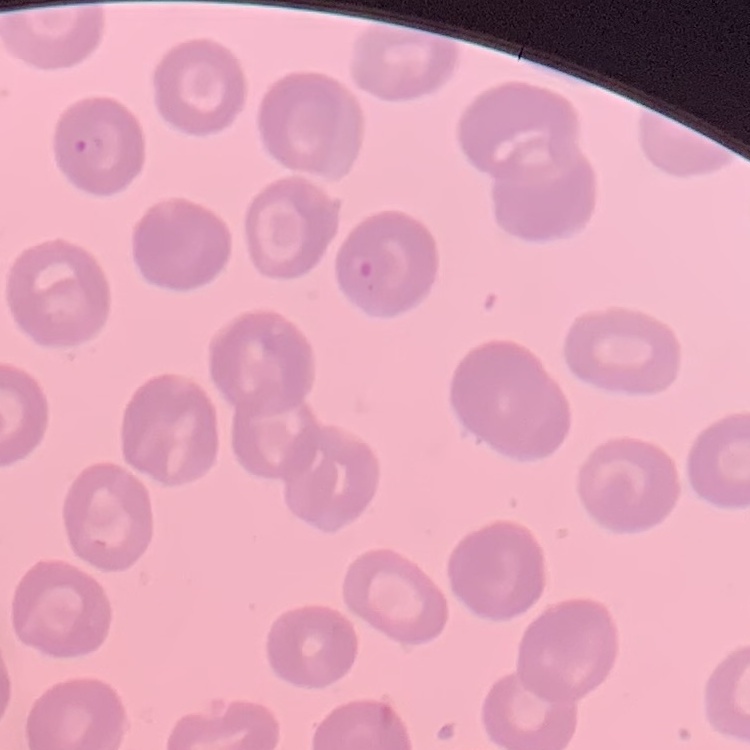 The red blood cells exhibit no rouleaux formation. Stained with either Field's or Giemsa. Thin peripheral smear. Square crop of a larger photomicrograph.